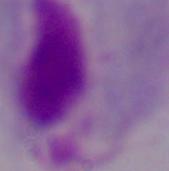
Photomicrograph. Captured at 1000x magnification. A trichomonad is shown.